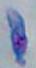

Summary:
  - Identification: Toxoplasma gondii
  - Modality: micrograph
  - Magnification: 1000x